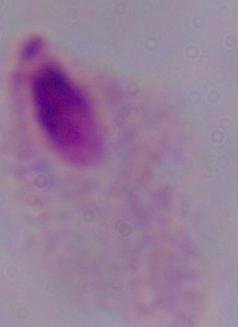
{
  "modality": "photomicrograph",
  "magnification": "1000x",
  "identification": "trichomonad"
}